Assess the morphology of the erythrocytes.
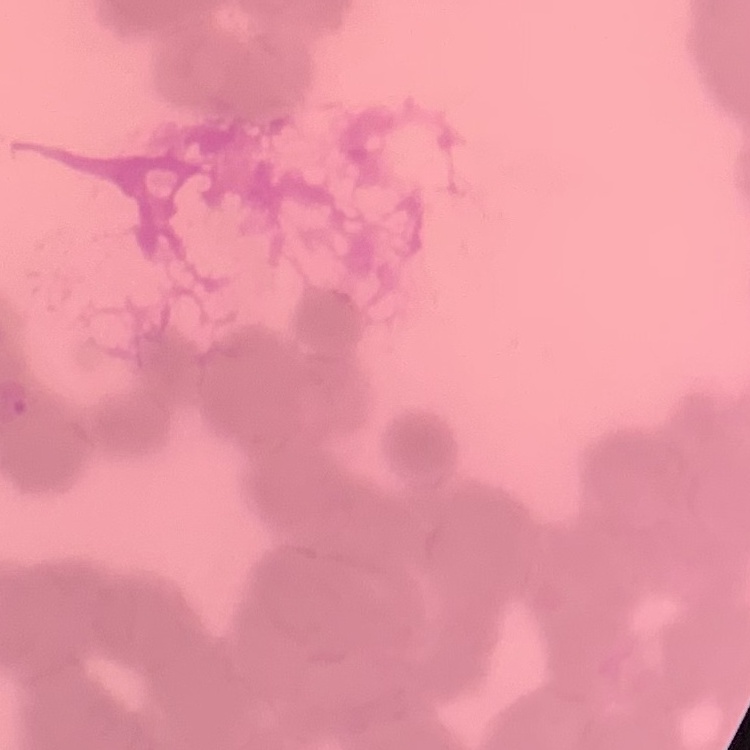
Rouleaux formation.

Summary:
  - Image type: one tile cut from a larger photomicrograph
  - Stain: Field's or Giemsa
  - Preparation: thin peripheral smear